Report the malaria status of this cell.
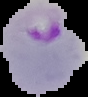

Parasitized.

Summary:
  - Image size: 88×97 pixels
  - Preparation: thin blood smear
  - Image type: segmented cell region with the area outside set to black